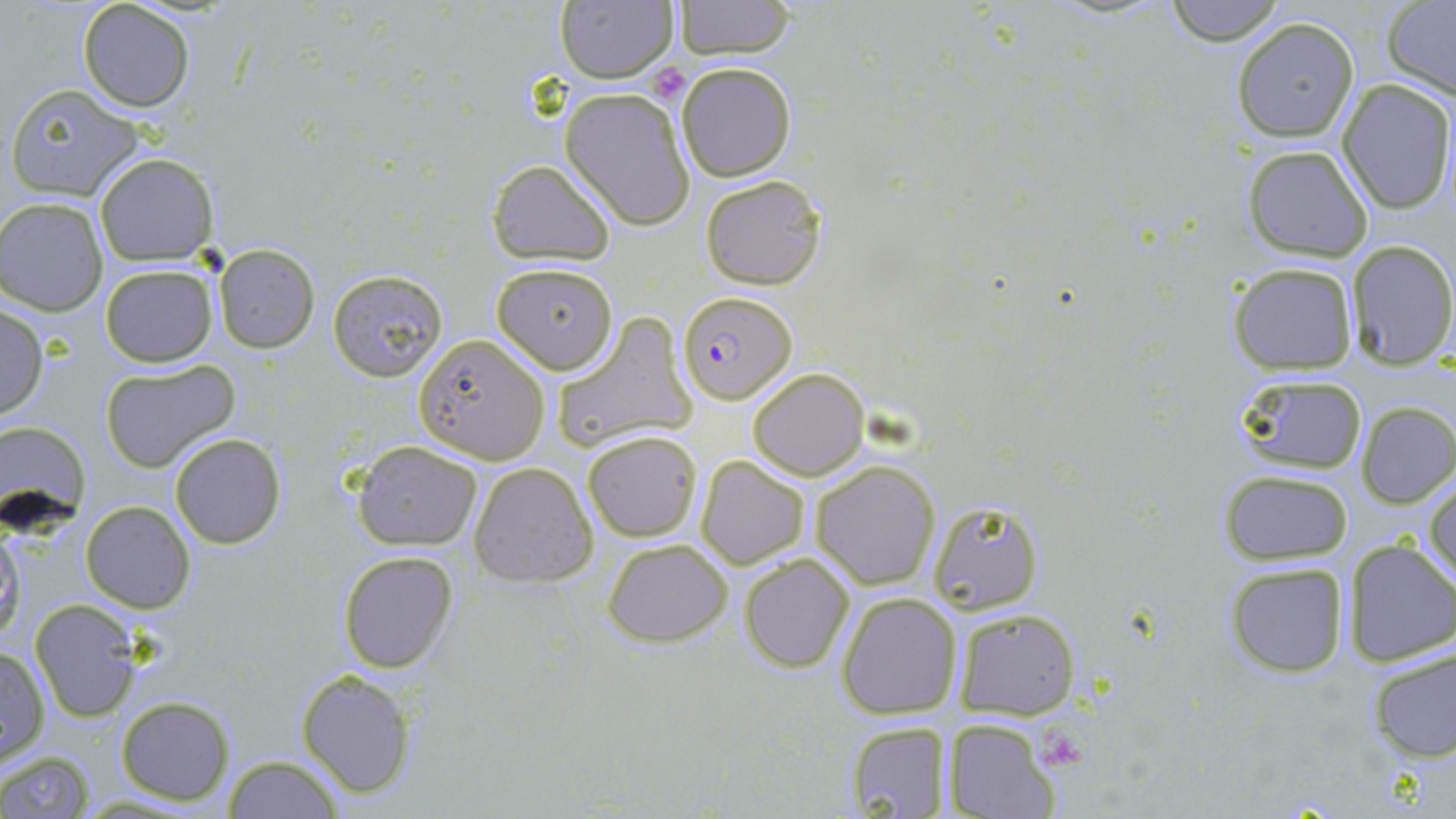

Approximate bounding boxes as (x1, y1, x2, y2) in pixels. Uninfected red blood cell locations: (554, 0, 677, 85), (76, 1, 195, 112), (673, 1, 797, 60), (1163, 1, 1286, 45), (1380, 1, 1456, 100), (1232, 19, 1359, 143), (676, 61, 797, 182), (1336, 78, 1456, 213), (6, 82, 145, 202), (559, 88, 694, 228), (1242, 144, 1375, 263), (94, 153, 217, 263), (488, 159, 615, 265), (700, 174, 828, 290), (2, 197, 111, 316), (1347, 238, 1456, 369), (214, 245, 319, 352), (490, 261, 619, 372), (1230, 261, 1359, 375), (100, 263, 218, 367), (328, 270, 447, 382), (0, 305, 49, 423), (551, 312, 697, 455), (412, 332, 551, 463), (99, 360, 241, 472), (747, 367, 869, 479), (1233, 372, 1369, 475), (1355, 401, 1455, 509), (0, 418, 92, 535), (582, 429, 702, 542), (169, 433, 286, 548), (354, 439, 483, 551), (695, 457, 811, 570), (811, 459, 940, 589), (469, 461, 598, 589), (1220, 470, 1354, 565), (1426, 475, 1456, 592), (81, 499, 196, 614), (924, 500, 1043, 614), (0, 523, 24, 650), (600, 538, 732, 647), (1339, 538, 1455, 668), (337, 551, 459, 674), (738, 551, 855, 673), (1222, 561, 1350, 677), (835, 592, 963, 720), (30, 601, 143, 722), (951, 605, 1080, 718), (1363, 644, 1456, 763), (0, 647, 50, 766), (296, 670, 415, 796), (115, 695, 235, 806), (843, 718, 955, 818), (944, 718, 1062, 819), (0, 751, 96, 819), (220, 756, 347, 817). Plasmodium falciparum-infected red blood cell locations: (678, 291, 796, 404). Platelet locations: (645, 65, 689, 105). Slide-level diagnosis: Plasmodium falciparum. Single field of view. Image is 1456×819 pixels. Thin blood film. Optical microscopy. May-Grünwald-Giemsa stain. Captured at 1000x magnification.